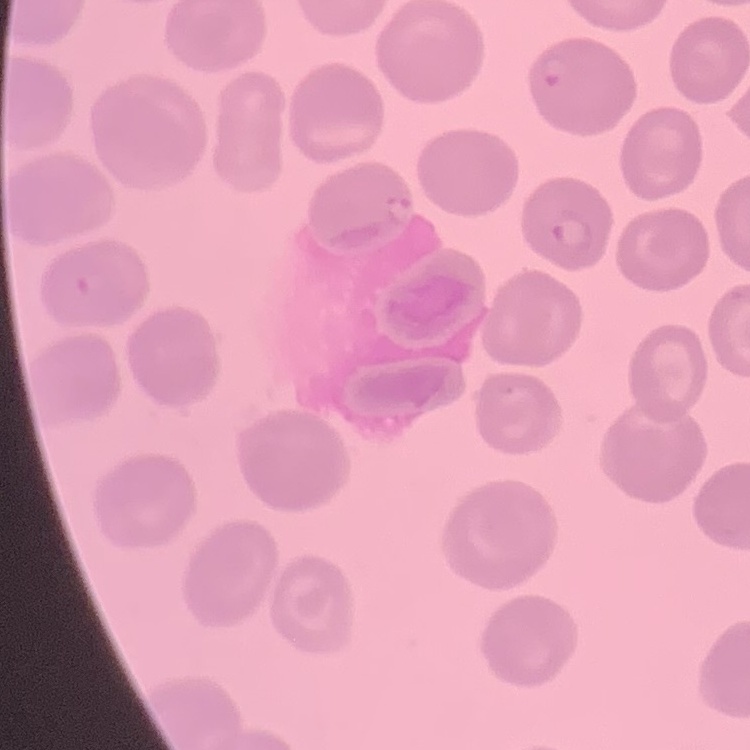

erythrocyte morphology = no rouleaux formation
preparation = thin peripheral smear
stain = Field's or Giemsa
image type = square crop of a larger photomicrograph